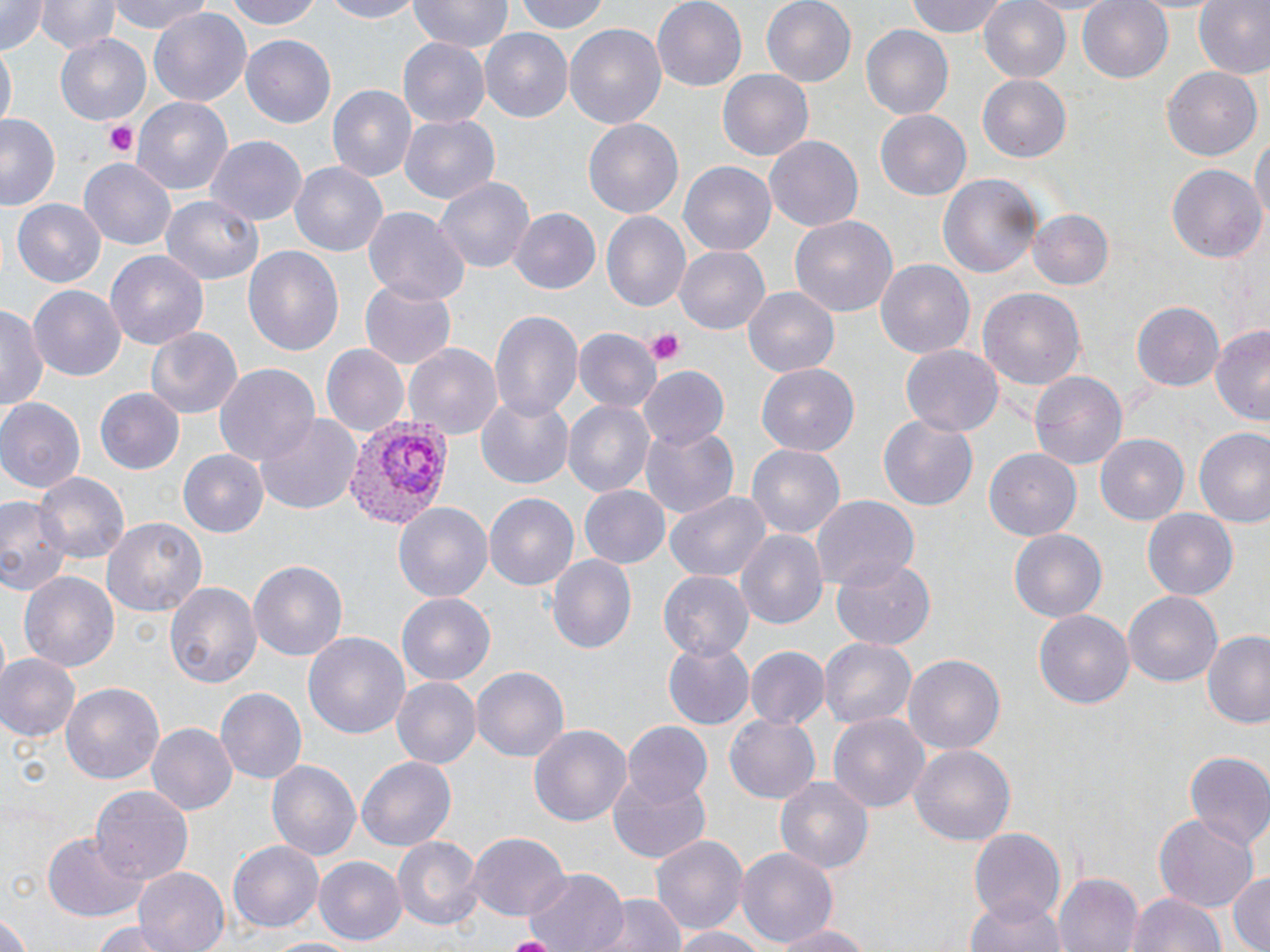
slide-level diagnosis = Plasmodium vivax
field of view = one of a larger specimen
preparation = thin blood smear
magnification = 1000x
platelet locations = approximate bounding boxes as (x1, y1, x2, y2) in pixels: (104, 119, 139, 157), (645, 331, 685, 366)
modality = optical microscopy
uninfected red blood cell locations = approximate bounding boxes as (x1, y1, x2, y2) in pixels: (0, 0, 48, 54), (39, 0, 118, 54), (108, 0, 209, 35), (229, 0, 325, 30), (318, 0, 429, 23), (408, 0, 511, 53), (515, 0, 610, 37), (652, 0, 748, 90), (761, 0, 858, 87), (902, 0, 1010, 39), (977, 0, 1073, 85), (1077, 0, 1175, 83), (1191, 1, 1270, 80), (148, 8, 251, 109), (564, 23, 665, 133), (861, 24, 953, 122), (481, 28, 574, 123), (54, 33, 152, 123), (240, 36, 336, 128), (399, 39, 489, 125), (1, 47, 14, 132), (1161, 65, 1261, 162), (717, 68, 813, 162), (977, 75, 1070, 162), (326, 86, 417, 184), (131, 96, 232, 197), (875, 109, 971, 201), (399, 112, 500, 203), (0, 113, 63, 209), (583, 118, 686, 220), (1250, 128, 1269, 235), (204, 136, 306, 227), (765, 136, 863, 229), (79, 160, 176, 248), (290, 161, 387, 257), (1166, 161, 1266, 263), (679, 162, 775, 256), (937, 172, 1044, 278), (434, 174, 535, 274), (162, 196, 263, 285), (11, 199, 106, 286), (363, 207, 469, 308), (1027, 208, 1115, 293), (509, 209, 601, 294), (600, 211, 691, 316), (791, 215, 898, 319), (243, 244, 344, 356), (676, 246, 768, 333), (104, 251, 210, 351), (875, 260, 975, 359), (359, 280, 457, 370), (979, 287, 1086, 391), (29, 288, 124, 380), (744, 288, 838, 375), (1130, 301, 1223, 394), (1, 302, 45, 421), (488, 310, 584, 423), (1210, 323, 1270, 424), (146, 328, 242, 420), (574, 329, 660, 410), (322, 344, 409, 437), (404, 344, 501, 441), (899, 345, 1004, 440), (215, 362, 319, 467), (756, 364, 860, 457), (640, 366, 730, 452), (1030, 370, 1130, 469), (94, 388, 183, 476), (478, 393, 573, 489), (0, 396, 86, 494), (563, 401, 656, 500), (255, 412, 362, 514), (878, 414, 980, 511), (640, 423, 738, 522), (1193, 427, 1270, 529), (1095, 433, 1192, 526), (747, 444, 845, 538), (984, 450, 1083, 541), (180, 451, 267, 536), (34, 473, 127, 567), (580, 486, 670, 569), (665, 491, 772, 584), (484, 492, 580, 591), (812, 494, 920, 593), (0, 495, 69, 598), (392, 502, 495, 605), (1141, 510, 1237, 599), (102, 517, 208, 620), (1009, 529, 1106, 622), (737, 530, 828, 631), (547, 553, 636, 653), (832, 557, 936, 650), (248, 559, 348, 663), (19, 570, 119, 669), (659, 571, 753, 662), (164, 578, 261, 687), (1123, 590, 1224, 689), (397, 592, 494, 688), (1035, 611, 1133, 711), (302, 631, 409, 739), (1200, 631, 1270, 730), (819, 635, 915, 729), (661, 641, 755, 728), (745, 646, 829, 730), (0, 653, 80, 743), (903, 653, 1005, 755), (471, 664, 567, 762), (391, 677, 480, 769), (61, 683, 164, 784), (215, 687, 307, 786), (829, 712, 929, 810), (724, 713, 819, 804), (147, 722, 237, 817), (623, 722, 713, 809), (529, 724, 630, 829), (910, 741, 1016, 847), (1184, 753, 1270, 854), (356, 756, 456, 853), (265, 759, 362, 864), (608, 774, 710, 863), (773, 776, 875, 875), (90, 785, 193, 885), (1155, 812, 1258, 911), (967, 829, 1067, 929), (467, 832, 569, 920), (649, 833, 750, 935), (42, 834, 146, 920), (391, 835, 483, 935), (228, 840, 324, 931), (736, 845, 838, 950), (314, 857, 405, 945), (134, 866, 231, 952), (524, 868, 626, 952), (1226, 871, 1269, 952), (1054, 874, 1143, 952), (1130, 892, 1224, 952), (599, 894, 687, 952), (963, 894, 1068, 952), (0, 906, 35, 951), (90, 921, 179, 952), (765, 923, 879, 950), (670, 927, 770, 952), (262, 936, 364, 952), (504, 937, 557, 950)
image size = 1270×952 pixels
stain = May-Grünwald-Giemsa
Plasmodium vivax-infected red blood cell locations = approximate bounding boxes as (x1, y1, x2, y2) in pixels: (346, 417, 452, 528)